Assess the morphology of the red blood cells.
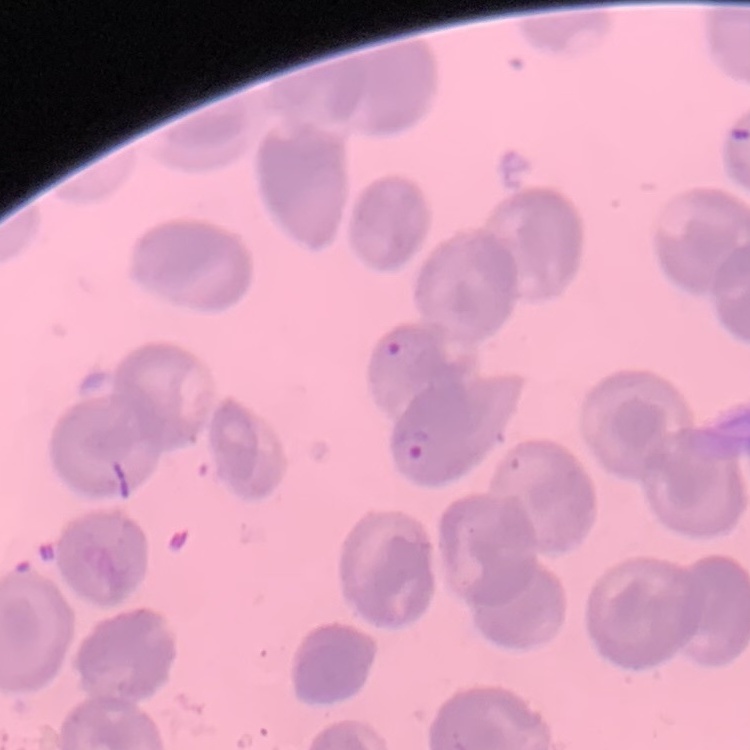
No rouleaux formation.

Square crop of a larger photomicrograph. Stained with either Field's or Giemsa. Thin blood smear.